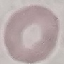

malaria_status: uninfected
capture: smartphone camera at the microscope eyepiece
image_type: cell patch, automatically extracted from a larger field of view and resized to 64 × 64 pixels
preparation: thin blood film
stain: Giemsa